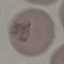
Malaria status: uninfected. Cell patch, automatically extracted from a larger field of view and resized to 64 × 64 pixels. Giemsa-stained preparation. Photographed with a smartphone camera at the microscope eyepiece. Thin smear of blood.